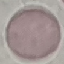
Summary:
  - Malaria status: uninfected
  - Preparation: thin blood film
  - Capture: smartphone through the microscope eyepiece
  - Stain: Giemsa
  - Image type: cell patch, automatically extracted from a larger field of view and resized to 64 × 64 pixels